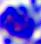

Summary:
  - Identification: leukocyte
  - Modality: micrograph
  - Magnification: 400x